Locate leukocytes (white blood cells).
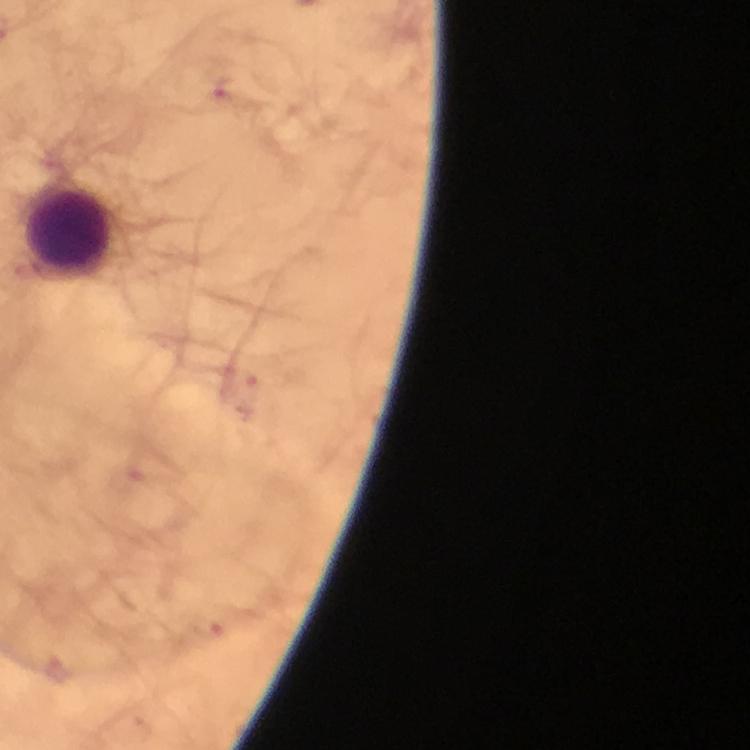

Approximate centers as {x, y} in pixels.
Leukocytes: {68, 233}.

Summary:
  - Malaria parasite locations: {220, 88}, {242, 382}, {206, 625}
  - Preparation: thick smear
  - Image size: 750×750 pixels
  - Immersion oil: applied
  - Magnification: 100x
  - Context: from a diagnostic examination for malaria
  - Capture: smartphone mounted on the microscope
  - Cropped from: a single field of view
  - Stain: Giemsa